Give the position of every Plasmodium parasite.
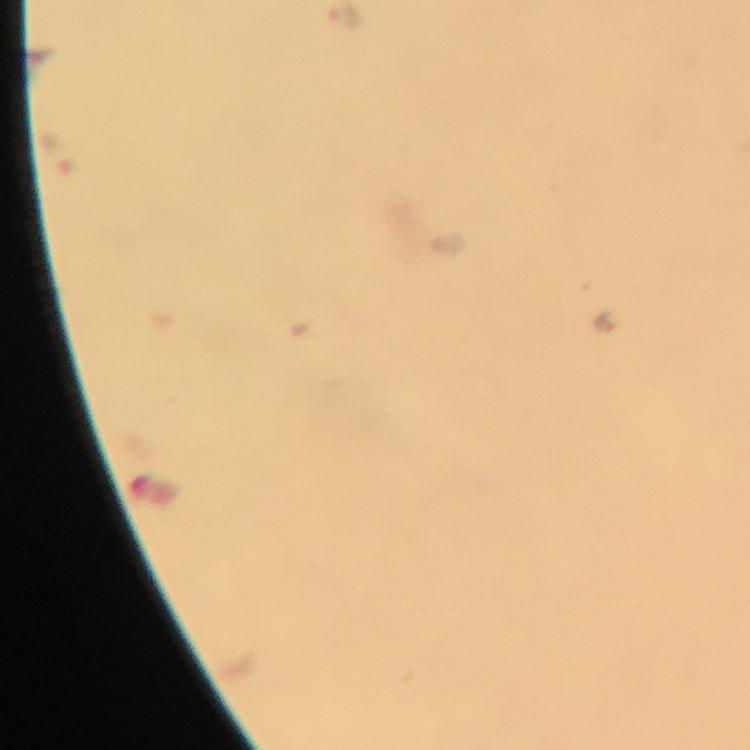

Approximate centers as [x, y] in pixels.
Plasmodium parasites: [345, 17], [605, 321].

immersion_oil: applied
magnification: 100x
cropped_from: one field of view
preparation: thick blood film
image_size: 750×750 pixels
capture: smartphone camera through the microscope
stain: Giemsa
context: from a diagnostic examination for malaria